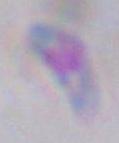

identification = Toxoplasma gondii
modality = micrograph
magnification = 1000x